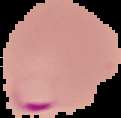
From a thin blood smear. Image is 121×118 pixels. The area outside the segmented cell region is set to black. Result: malaria parasites detected.